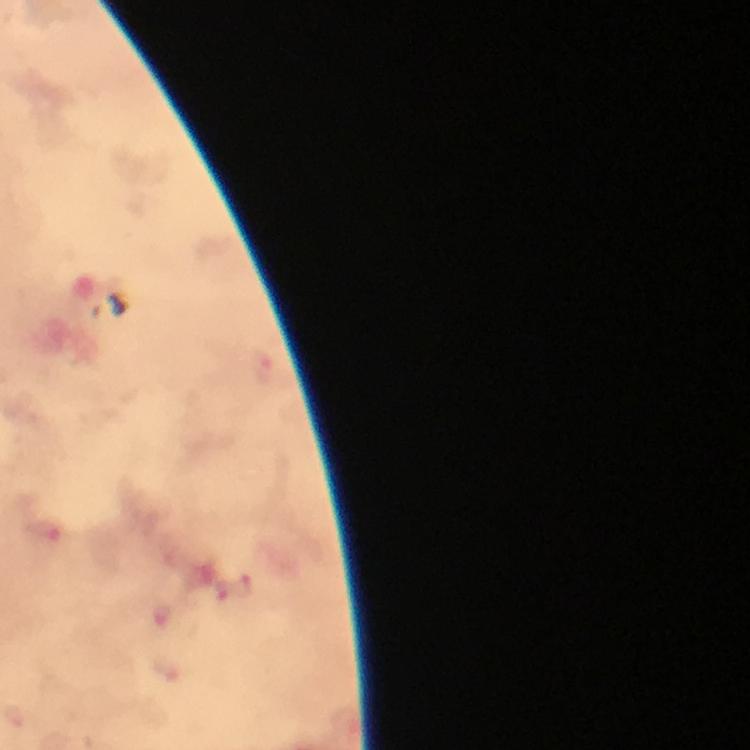 Approximate centers as {x, y} in pixels. Malaria parasite locations: {234, 593}. 100x magnification. Immersion oil applied. Cropped region of a single field of view. Thick blood smear. Image is 750×750 pixels. Giemsa-stained preparation. From a malaria diagnostic workup. Photographed through the microscope with a smartphone camera.